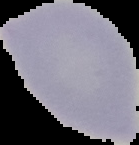

result = negative for malaria parasites
preparation = thin blood smear
image size = 139×145 pixels
image type = cell region segmented out of the field of view; surrounding area masked to black